Assess this cell for malaria.
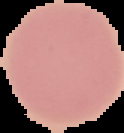

It is uninfected.

Cell region segmented out of the field of view; the surrounding area is masked to black. Image is 124×133 pixels. From a thin blood film.